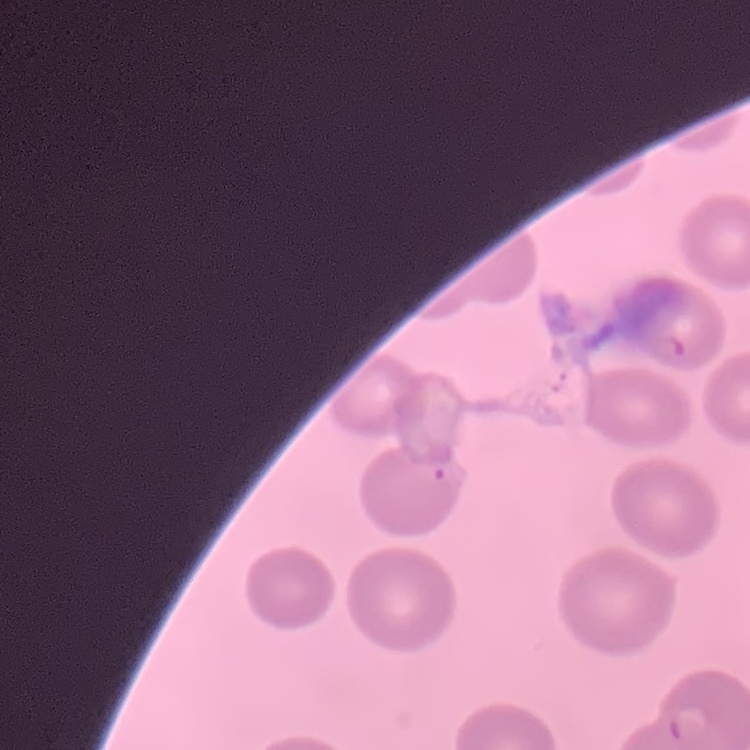

erythrocyte morphology = no rouleaux formation
stain = Field's or Giemsa
image type = one tile cut from a larger photomicrograph
preparation = thin peripheral smear